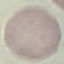
Summary:
  - Malaria status: uninfected
  - Image type: automatically extracted cell patch, resized to 64 × 64 pixels
  - Stain: Giemsa
  - Capture: smartphone camera at the microscope eyepiece
  - Preparation: thin blood film